State which parasite is depicted.
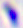
Toxoplasma gondii.

{
  "magnification": "400x",
  "modality": "micrograph"
}